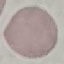
malaria status = uninfected
preparation = thin blood smear
image type = automatically extracted cell patch, resized to 64 × 64 pixels
capture = smartphone through the microscope eyepiece
stain = Giemsa